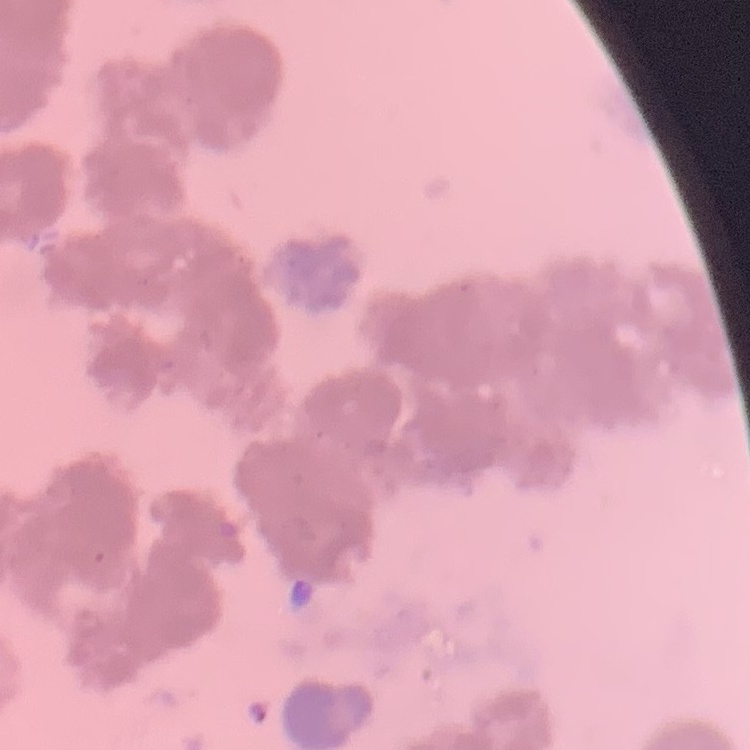
The erythrocytes exhibit rouleaux formation. Thin peripheral smear. Stained with either Field's or Giemsa. Square crop of a larger photomicrograph.